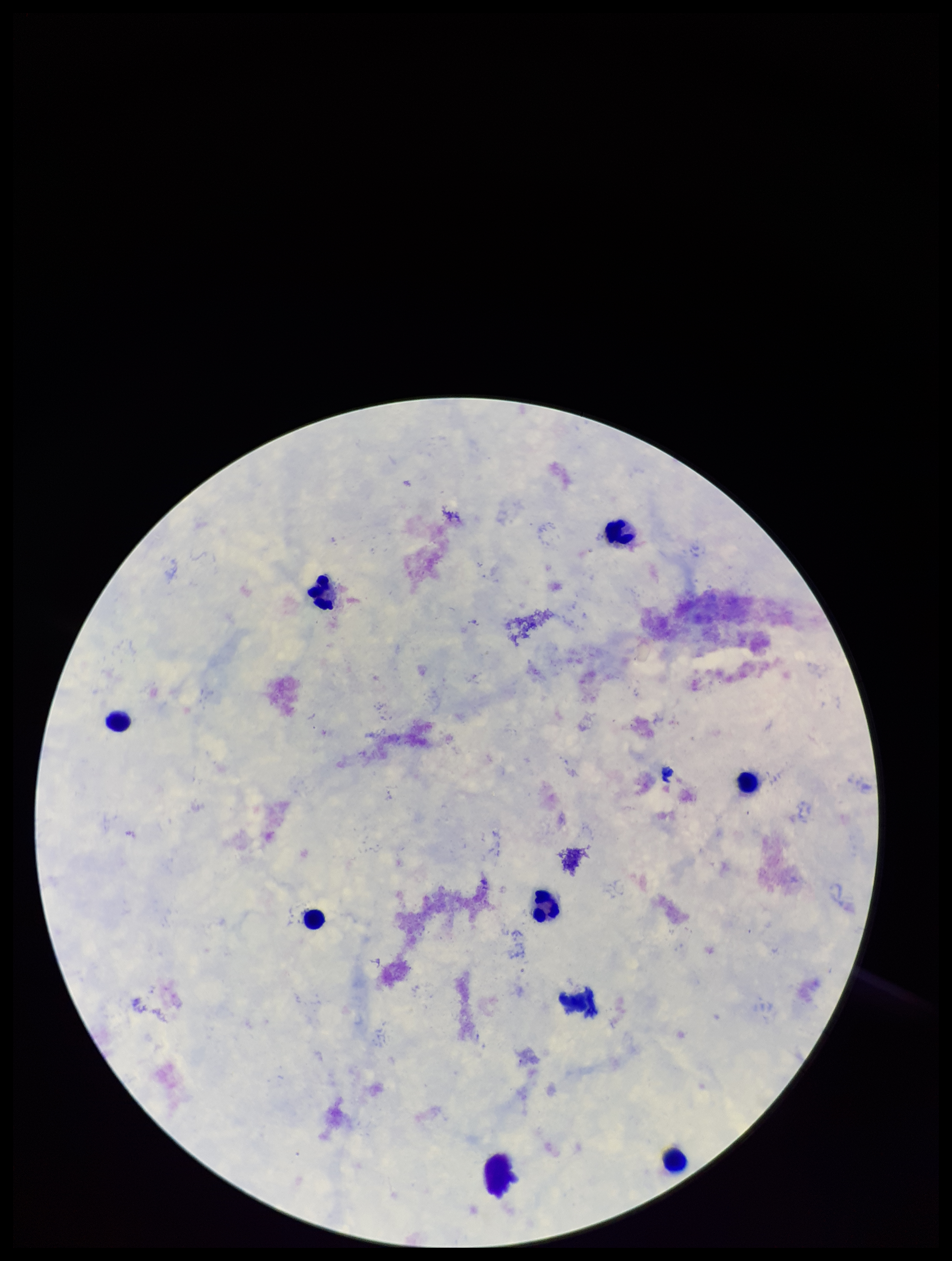
Summary:
  - Parasite count: 0
  - Capture: smartphone photograph through the microscope eyepiece
  - Plasmodium parasites: none seen
  - Leukocyte count: 9
  - Preparation: thick smear
  - Stain: Giemsa
  - Field of view: one from this slide
  - Patient malaria status: negative
  - Image size: 952×1261 pixels